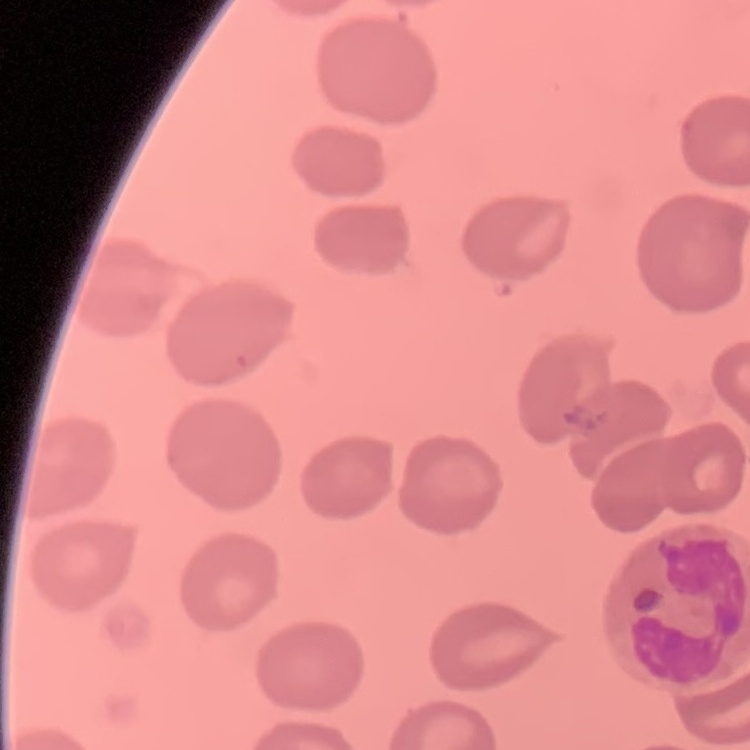
{
  "red_blood_cell_morphology": "no rouleaux formation",
  "stain": "Field's or Giemsa",
  "image_type": "one tile cut from a larger photomicrograph",
  "preparation": "thin blood smear"
}